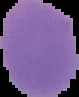

Summary:
  - Malaria status: uninfected
  - Image size: 79×97 pixels
  - Image type: segmented cell region on a black background
  - Preparation: thin blood film